Classify this cell by malaria status.
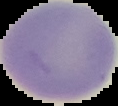

Uninfected.

{
  "preparation": "thin blood smear",
  "image_type": "segmented cell region on a black background",
  "image_size": "118×106 pixels"
}